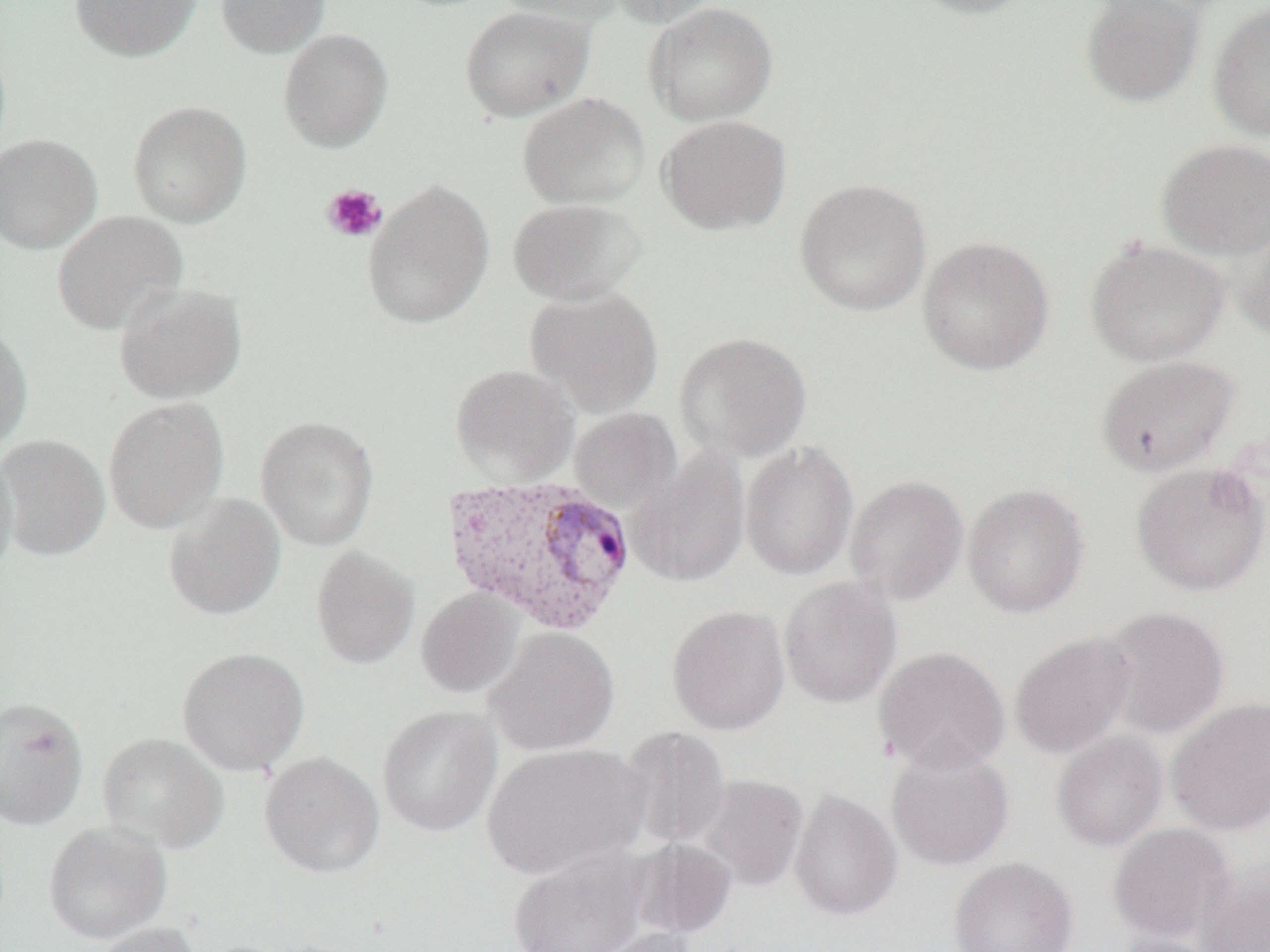
Summary:
  - Coordinate format: approximate bounding boxes as (x1, y1, x2, y2) in pixels
  - Platelet locations: (321, 183, 387, 243)
  - Uninfected red blood cell locations: (69, 0, 202, 62), (216, 0, 330, 57), (491, 0, 626, 26), (605, 0, 725, 28), (905, 0, 1036, 20), (1079, 0, 1204, 108), (643, 1, 778, 126), (1208, 3, 1270, 141), (460, 5, 593, 122), (278, 28, 394, 153), (518, 92, 650, 209), (127, 100, 252, 228), (657, 114, 792, 236), (0, 133, 102, 254), (1156, 138, 1270, 260), (362, 178, 495, 330), (794, 178, 932, 316), (507, 198, 645, 306), (52, 210, 188, 335), (1235, 222, 1270, 339), (917, 235, 1055, 375), (1085, 237, 1230, 367), (114, 282, 248, 404), (525, 287, 664, 417), (0, 322, 33, 450), (674, 331, 813, 462), (1096, 354, 1239, 476), (449, 363, 580, 485), (103, 396, 229, 534), (568, 408, 682, 515), (255, 415, 379, 551), (0, 434, 110, 561), (740, 440, 859, 581), (0, 444, 19, 580), (629, 447, 751, 588), (1131, 461, 1270, 596), (845, 474, 969, 606), (962, 483, 1090, 618), (163, 493, 286, 621), (311, 544, 420, 669), (779, 576, 902, 708), (416, 588, 524, 698), (666, 604, 791, 736), (1097, 605, 1230, 739), (485, 627, 619, 757), (1010, 631, 1136, 759), (177, 646, 309, 776), (873, 646, 1010, 774), (0, 696, 89, 830), (1166, 697, 1270, 835), (377, 706, 502, 837), (620, 726, 732, 850), (1051, 731, 1168, 852), (97, 732, 229, 854), (885, 742, 1015, 871), (481, 743, 646, 881), (259, 751, 384, 878), (696, 774, 809, 892), (789, 789, 902, 921), (43, 820, 173, 945), (1108, 822, 1235, 945), (627, 838, 738, 940), (506, 844, 654, 952), (949, 856, 1079, 952), (1196, 863, 1270, 952), (88, 922, 201, 952), (577, 926, 705, 952), (1113, 934, 1226, 952)
  - Plasmodium vivax-infected red blood cell locations: (441, 473, 637, 636)
  - Slide-level diagnosis: Plasmodium vivax
  - Modality: optical microscopy
  - Magnification: 1000x
  - Image size: 1270×952 pixels
  - Field of view: one of a larger specimen
  - Preparation: thin blood smear